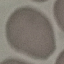
result: no malaria parasites detected
image_type: cell patch, automatically extracted from a larger field of view and resized to 64 × 64 pixels
capture: smartphone through the microscope eyepiece
stain: Giemsa
preparation: thin blood smear